Locate every leukocyte (white blood cell).
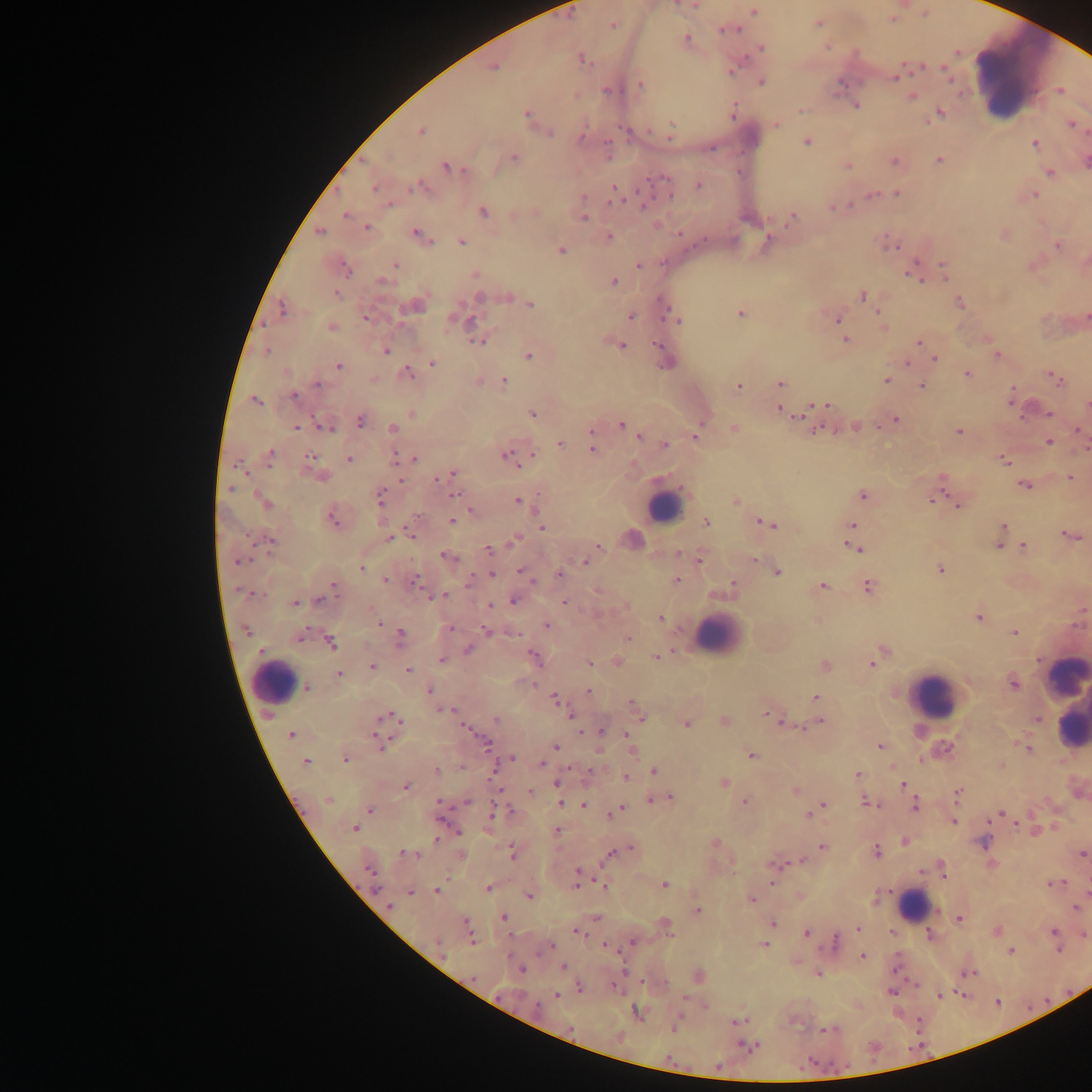
Approximate centers as [x, y] in pixels.
Leukocytes: [1021, 77], [664, 505], [716, 635], [1067, 676], [275, 682], [932, 694], [1069, 715], [913, 905].

Summary:
  - Malaria parasite locations: [695, 5], [754, 12], [818, 22], [613, 25], [730, 30], [686, 38], [761, 48], [582, 59], [493, 67], [945, 69], [733, 70], [897, 76], [762, 82], [840, 83], [640, 85], [606, 90], [1061, 91], [912, 97], [856, 106], [801, 109], [733, 113], [939, 113], [526, 114], [776, 124], [1071, 124], [421, 130], [628, 131], [670, 131], [550, 133], [581, 136], [806, 142], [1035, 144], [607, 150], [514, 157], [939, 159], [1086, 161], [894, 162], [847, 165], [447, 167], [1050, 172], [663, 178], [698, 185], [375, 187], [417, 187], [898, 193], [669, 195], [1034, 195], [615, 196], [872, 196], [583, 198], [833, 207], [848, 207], [483, 212], [346, 215], [583, 219], [791, 219], [366, 227], [319, 232], [680, 233], [417, 234], [609, 237], [461, 241], [768, 242], [891, 245], [1058, 246], [561, 250], [395, 265], [638, 266], [943, 267], [346, 268], [476, 273], [913, 275], [614, 281], [382, 282], [336, 294], [863, 295], [480, 297], [508, 297], [960, 303], [531, 304], [663, 305], [416, 306], [283, 308], [670, 313], [740, 314], [631, 316], [366, 318], [1087, 318], [468, 320], [838, 320], [678, 321], [883, 327], [331, 328], [845, 340], [477, 342], [919, 342], [658, 345], [621, 346], [267, 351], [386, 351], [997, 354], [529, 355], [935, 359], [432, 363], [666, 364], [338, 366], [406, 373], [968, 375], [886, 380], [1056, 380], [503, 381], [780, 383], [318, 384], [921, 386], [739, 387], [294, 396], [1011, 399], [256, 401], [820, 405], [1087, 405], [811, 408], [781, 410], [1049, 413], [411, 414], [533, 414], [796, 414], [895, 420], [360, 421], [621, 425], [325, 427], [856, 427], [296, 428], [392, 428], [733, 428], [630, 430], [1079, 431], [958, 432], [591, 435], [696, 435], [639, 436], [1049, 442], [665, 444], [560, 445], [593, 449], [271, 453], [532, 456], [310, 457], [507, 457], [396, 458], [413, 458], [349, 459], [1004, 460], [238, 465], [452, 474], [441, 476], [1070, 478], [941, 483], [1025, 486], [230, 488], [455, 495], [862, 495], [935, 497], [381, 498], [518, 501], [736, 501], [266, 503], [959, 506], [470, 512], [332, 519], [452, 521], [761, 521], [706, 522], [768, 524], [852, 525], [1003, 526], [541, 527], [411, 533], [1071, 536], [389, 537], [271, 540], [513, 541], [598, 546], [999, 546], [1024, 546], [852, 547], [488, 550], [446, 556], [699, 559], [754, 559], [238, 560], [585, 562], [361, 568], [940, 569], [777, 572], [524, 574], [560, 574], [492, 575], [385, 580], [415, 581], [676, 581], [732, 584], [334, 585], [823, 586], [867, 587], [442, 596], [319, 600], [513, 601], [564, 602], [295, 603], [489, 606], [661, 618], [979, 618], [379, 622], [547, 626], [450, 628], [486, 630], [245, 631], [514, 633], [1014, 633], [401, 635], [300, 636], [628, 638], [331, 644], [468, 649], [882, 652], [657, 656], [535, 657], [442, 660], [618, 661], [589, 662], [872, 663], [825, 666], [372, 667], [408, 670], [339, 675], [1013, 683], [307, 688], [588, 690], [430, 691], [816, 697], [555, 699], [634, 707], [445, 711], [770, 714], [640, 716], [382, 718], [397, 718], [571, 718], [496, 719], [778, 719], [725, 721], [820, 721], [686, 724], [602, 732], [290, 735], [628, 735], [377, 738], [484, 743], [879, 745], [555, 746], [1026, 748], [631, 750], [751, 755], [511, 758], [345, 760], [305, 763], [541, 764], [436, 770], [590, 770], [654, 772], [858, 775], [626, 777], [556, 783], [724, 783], [902, 784], [406, 786], [796, 791], [530, 792], [958, 793], [669, 798], [327, 799], [653, 799], [745, 801], [468, 802], [441, 803], [867, 803], [561, 804], [823, 805], [584, 806], [915, 806], [620, 809], [370, 810], [815, 811], [498, 812], [998, 814], [954, 822], [354, 828], [558, 831], [437, 840], [905, 841], [715, 843], [983, 843], [823, 847], [630, 849], [876, 851], [512, 852], [406, 853], [1083, 853], [612, 854], [801, 860], [774, 866], [369, 871], [942, 871], [579, 874], [1051, 883], [604, 886], [665, 886], [488, 888], [437, 892], [411, 893], [530, 895], [752, 900], [389, 906], [1075, 908], [697, 910], [504, 917], [959, 919], [465, 922], [772, 923], [665, 924], [858, 928], [997, 931], [579, 933], [807, 933], [1054, 933], [469, 934], [1085, 935], [930, 936], [471, 940], [633, 942], [835, 942], [437, 943], [764, 944], [548, 948], [1058, 948], [1010, 950], [863, 956], [564, 967], [521, 969], [970, 973], [819, 974], [698, 975], [580, 988], [891, 991], [939, 995], [556, 996], [636, 1013], [737, 1021], [676, 1024], [829, 1030], [747, 1045], [811, 1063], [718, 1066]
  - Capture: mobile-phone photograph through a microscope
  - Preparation: thick blood film
  - Country: Ghana
  - Field of view: single
  - Image size: 1092×1092 pixels